Describe the morphology of the erythrocytes.
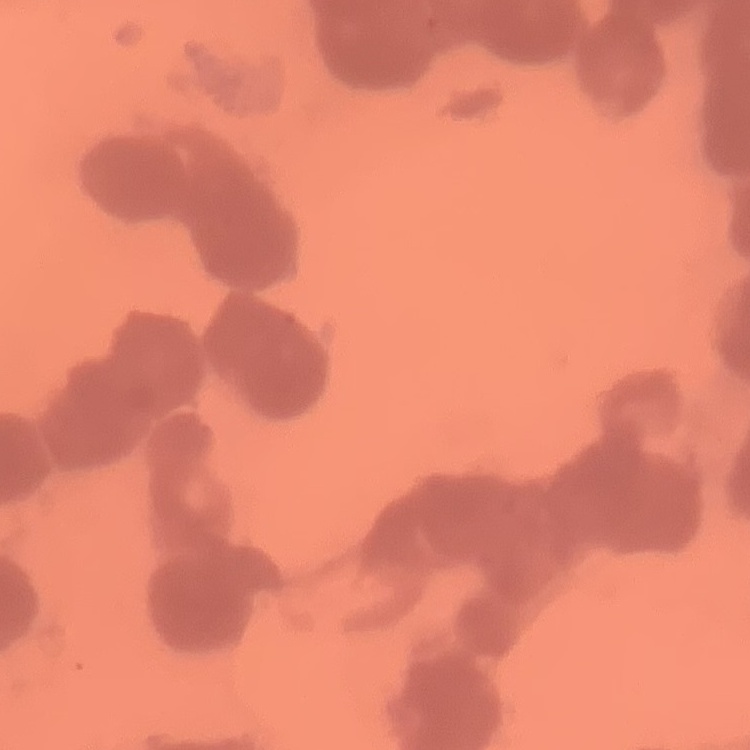

They show rouleaux formation.

preparation = thin blood smear
image type = one tile cut from a larger photomicrograph
stain = Field's or Giemsa